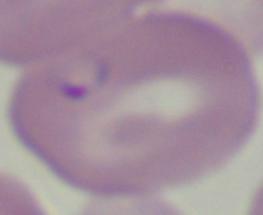

1000x magnification. A Babesia parasite is seen. Micrograph.